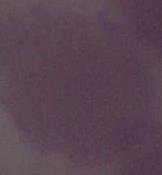
modality = photomicrograph
magnification = 1000x
identification = erythrocyte